Name the parasite shown.
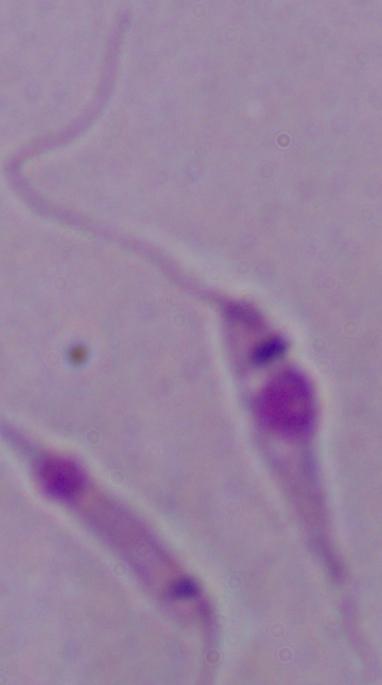
This is Leishmania.

modality = photomicrograph
magnification = 1000x